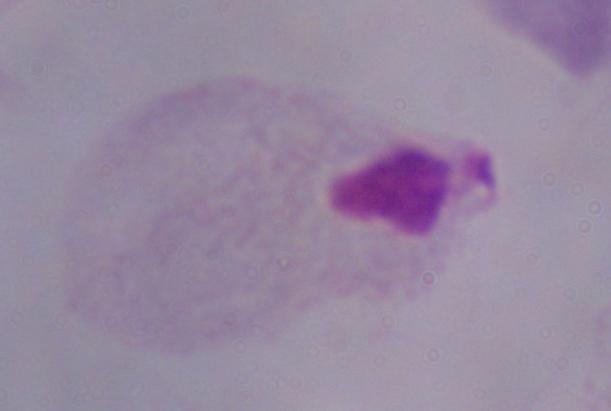
identification: trichomonad
modality: photomicrograph
magnification: 1000x